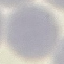

Summary:
  - Result: no malaria parasites detected
  - Preparation: thin blood smear
  - Capture: smartphone through the microscope eyepiece
  - Stain: Giemsa
  - Image type: automatically extracted cell patch, resized to 64 × 64 pixels